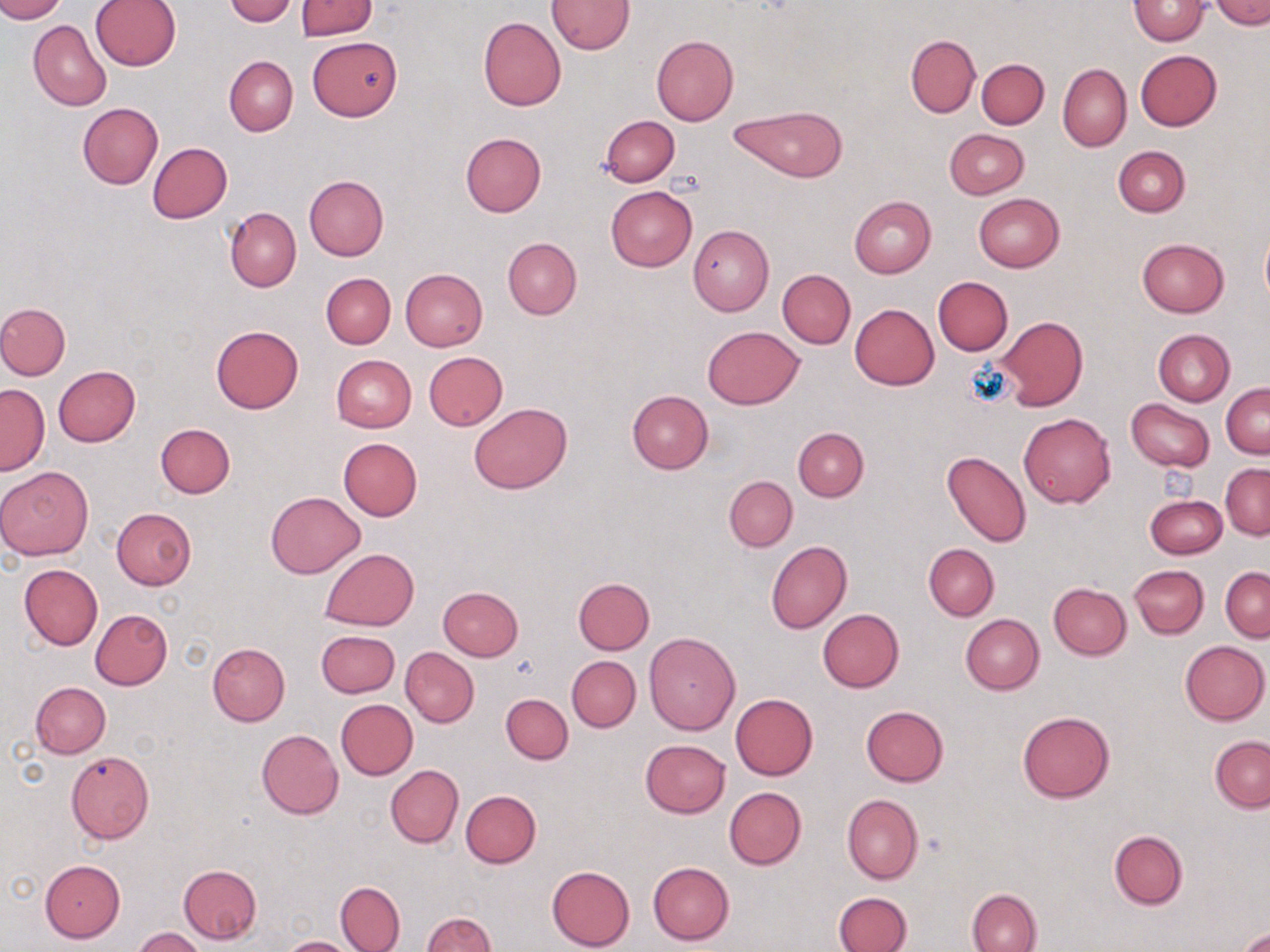
Approximate bounding boxes as (x1,y1)-(x2,y2) corner pairs in pixels. Uninfected red blood cell locations: (0,0)-(65,22), (224,0)-(297,26), (1129,0)-(1208,44), (91,1)-(181,71), (296,1)-(377,39), (547,1)-(634,54), (1209,1)-(1270,27), (478,17)-(566,111), (29,21)-(111,112), (651,35)-(738,126), (906,35)-(980,117), (307,37)-(403,121), (1136,50)-(1222,131), (225,55)-(297,136), (977,59)-(1048,128), (1058,64)-(1131,152), (78,102)-(163,189), (729,105)-(848,183), (600,114)-(679,186), (945,129)-(1030,199), (461,131)-(546,216), (147,143)-(232,224), (1114,146)-(1191,216), (304,176)-(388,260), (605,185)-(698,272), (974,194)-(1064,272), (850,195)-(936,277), (225,208)-(301,292), (687,225)-(774,315), (1261,229)-(1270,306), (503,238)-(581,318), (1136,238)-(1230,317), (400,269)-(488,351), (777,269)-(856,349), (321,273)-(395,348), (932,276)-(1012,354), (0,303)-(71,380), (850,304)-(939,389), (996,316)-(1088,410), (211,326)-(302,413), (703,326)-(804,408), (1153,329)-(1234,406), (424,352)-(507,431), (332,355)-(416,432), (54,366)-(141,447), (1221,382)-(1269,459), (0,384)-(49,474), (627,391)-(712,474), (1126,398)-(1215,471), (469,403)-(572,494), (1019,412)-(1115,508), (155,423)-(235,498), (793,427)-(869,501), (338,438)-(422,521), (942,451)-(1032,547), (1221,463)-(1270,540), (0,466)-(92,560), (725,475)-(798,552), (265,491)-(365,578), (1145,494)-(1226,560), (113,508)-(196,590), (766,541)-(853,633), (924,543)-(999,620), (320,549)-(419,630), (18,564)-(102,650), (1129,565)-(1209,638), (1221,566)-(1269,641), (574,577)-(655,654), (1049,583)-(1131,660), (438,586)-(523,661), (91,609)-(172,690), (818,609)-(904,692), (961,615)-(1044,694), (316,630)-(399,697), (644,632)-(742,735), (1181,640)-(1269,724), (207,642)-(290,726), (400,648)-(479,727), (567,656)-(641,731), (30,681)-(111,758), (501,692)-(572,763), (731,693)-(817,780), (336,699)-(417,780), (861,705)-(949,786), (1017,711)-(1116,803), (256,729)-(344,819), (1211,735)-(1270,811), (640,739)-(731,817), (66,751)-(154,843), (386,765)-(464,847), (725,787)-(806,870), (461,790)-(541,868), (842,794)-(923,885), (1109,829)-(1188,909), (40,859)-(125,942), (647,861)-(735,945), (179,864)-(262,943), (546,864)-(635,952), (336,882)-(405,951), (967,889)-(1043,951), (835,891)-(913,952), (422,912)-(498,952), (133,927)-(204,952), (1239,928)-(1270,951), (278,936)-(357,952). Platelet locations: (670,169)-(706,195), (511,652)-(542,682), (924,830)-(951,858). Slide-level diagnosis: no evidence of blood parasites. Single field of view. 1000x magnification. Image is 1270×952 pixels. May-Grünwald-Giemsa-stained preparation. Optical microscopy. Thin blood smear.